Evaluate for Plasmodium parasites.
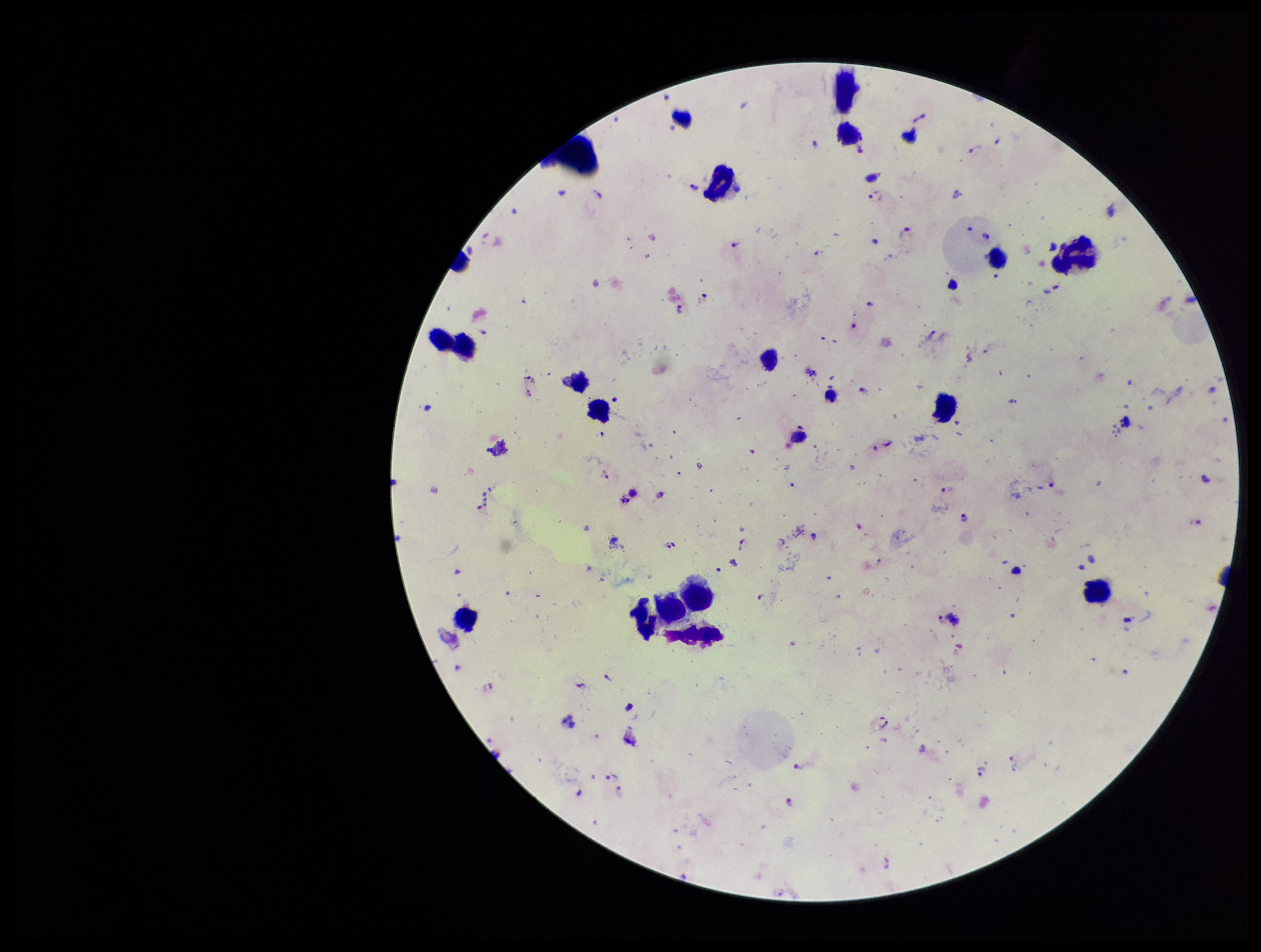

Seen.

{
  "capture": "smartphone photograph through the microscope eyepiece",
  "leukocyte_count": 15,
  "patient_malaria_status": "infected",
  "stain": "Giemsa",
  "parasite_count": 32,
  "image_size": "1261×952 pixels",
  "species_reported_for_this_patient": "Plasmodium falciparum",
  "preparation": "thick smear",
  "field_of_view": "single"
}